Name the parasite shown.
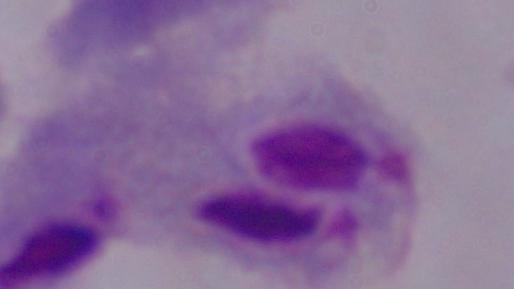

This is a trichomonad.

Captured at 1000x magnification. Micrograph.